Locate every Plasmodium falciparum-infected red blood cell.
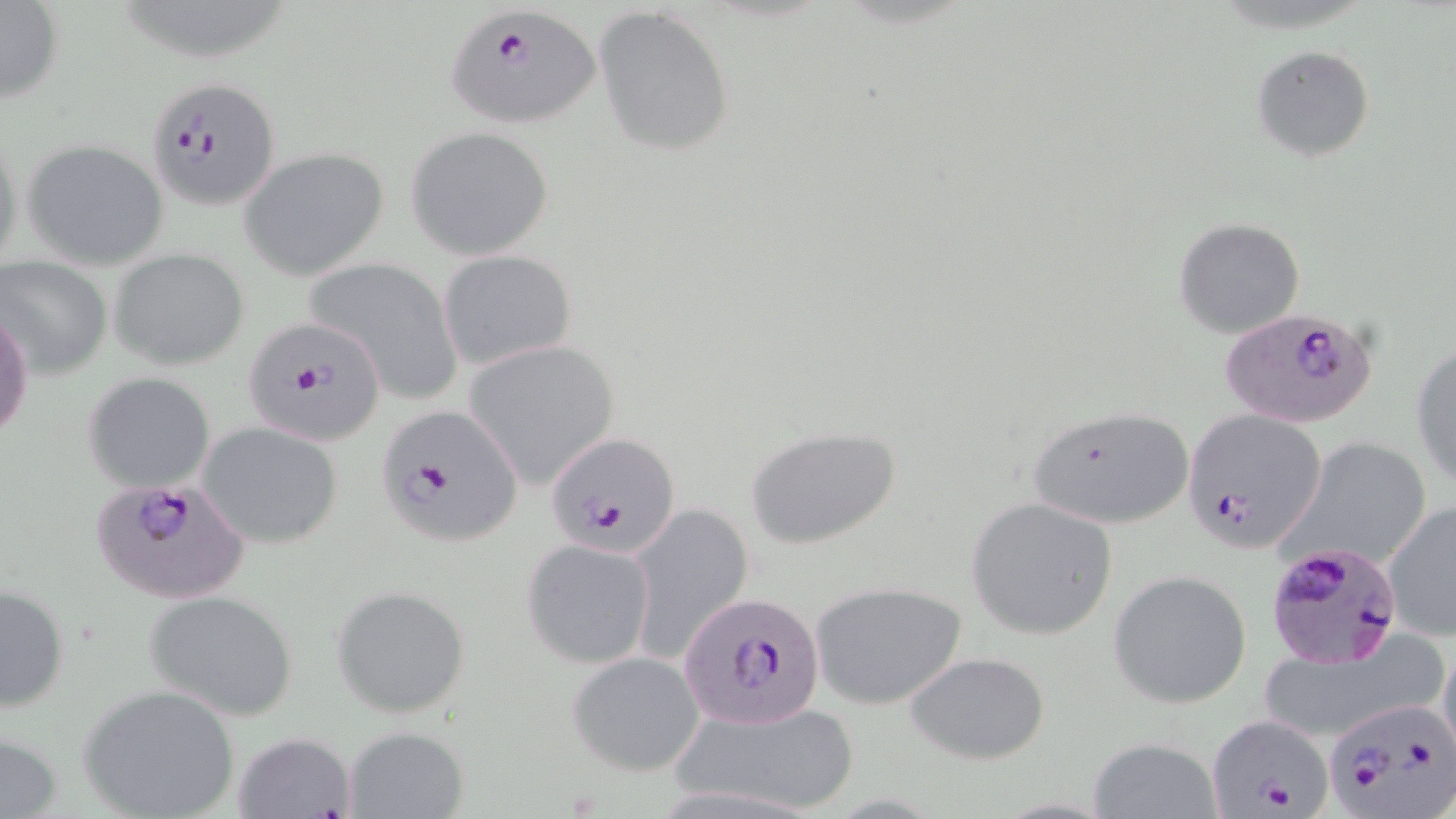
Approximate bounding boxes as named x1/y1/x2/y2 corners in pixels.
Plasmodium falciparum-infected red blood cells: (x1=445, y1=8, x2=600, y2=129), (x1=145, y1=74, x2=281, y2=211), (x1=1220, y1=306, x2=1377, y2=428), (x1=242, y1=317, x2=387, y2=445), (x1=373, y1=403, x2=524, y2=549), (x1=1181, y1=407, x2=1328, y2=555), (x1=545, y1=432, x2=680, y2=556), (x1=86, y1=477, x2=252, y2=603), (x1=1266, y1=538, x2=1404, y2=669), (x1=679, y1=593, x2=824, y2=724), (x1=1322, y1=698, x2=1456, y2=817), (x1=1206, y1=711, x2=1336, y2=817).

slide-level diagnosis = Plasmodium falciparum
stain = May-Grünwald-Giemsa
magnification = 1000x
field of view = single
preparation = thin blood smear
image size = 1456×819 pixels
modality = optical microscopy
uninfected red blood cell locations = approximate bounding boxes as named x1/y1/x2/y2 corners in pixels: (x1=0, y1=1, x2=63, y2=104), (x1=592, y1=8, x2=737, y2=156), (x1=1251, y1=45, x2=1375, y2=162), (x1=0, y1=122, x2=23, y2=277), (x1=407, y1=126, x2=555, y2=260), (x1=22, y1=137, x2=170, y2=270), (x1=240, y1=148, x2=388, y2=280), (x1=1172, y1=215, x2=1305, y2=339), (x1=110, y1=247, x2=251, y2=371), (x1=438, y1=249, x2=577, y2=369), (x1=1, y1=256, x2=111, y2=377), (x1=304, y1=257, x2=464, y2=405), (x1=1, y1=311, x2=34, y2=443), (x1=462, y1=341, x2=620, y2=487), (x1=1411, y1=341, x2=1456, y2=491), (x1=83, y1=371, x2=215, y2=492), (x1=1029, y1=405, x2=1195, y2=531), (x1=199, y1=421, x2=343, y2=549), (x1=747, y1=424, x2=903, y2=551), (x1=1283, y1=437, x2=1433, y2=573), (x1=967, y1=498, x2=1118, y2=639), (x1=1382, y1=500, x2=1456, y2=641), (x1=626, y1=501, x2=752, y2=664), (x1=521, y1=537, x2=655, y2=670), (x1=1108, y1=570, x2=1252, y2=708), (x1=807, y1=582, x2=968, y2=709), (x1=1, y1=584, x2=71, y2=713), (x1=333, y1=585, x2=469, y2=718), (x1=146, y1=589, x2=299, y2=720), (x1=1250, y1=639, x2=1446, y2=744), (x1=1437, y1=642, x2=1455, y2=768), (x1=902, y1=649, x2=1051, y2=764), (x1=567, y1=651, x2=705, y2=776), (x1=79, y1=682, x2=239, y2=819), (x1=668, y1=699, x2=860, y2=816), (x1=342, y1=726, x2=471, y2=819), (x1=1, y1=729, x2=62, y2=819), (x1=232, y1=731, x2=357, y2=819), (x1=1089, y1=736, x2=1222, y2=818)